Identify the blood parasite species.
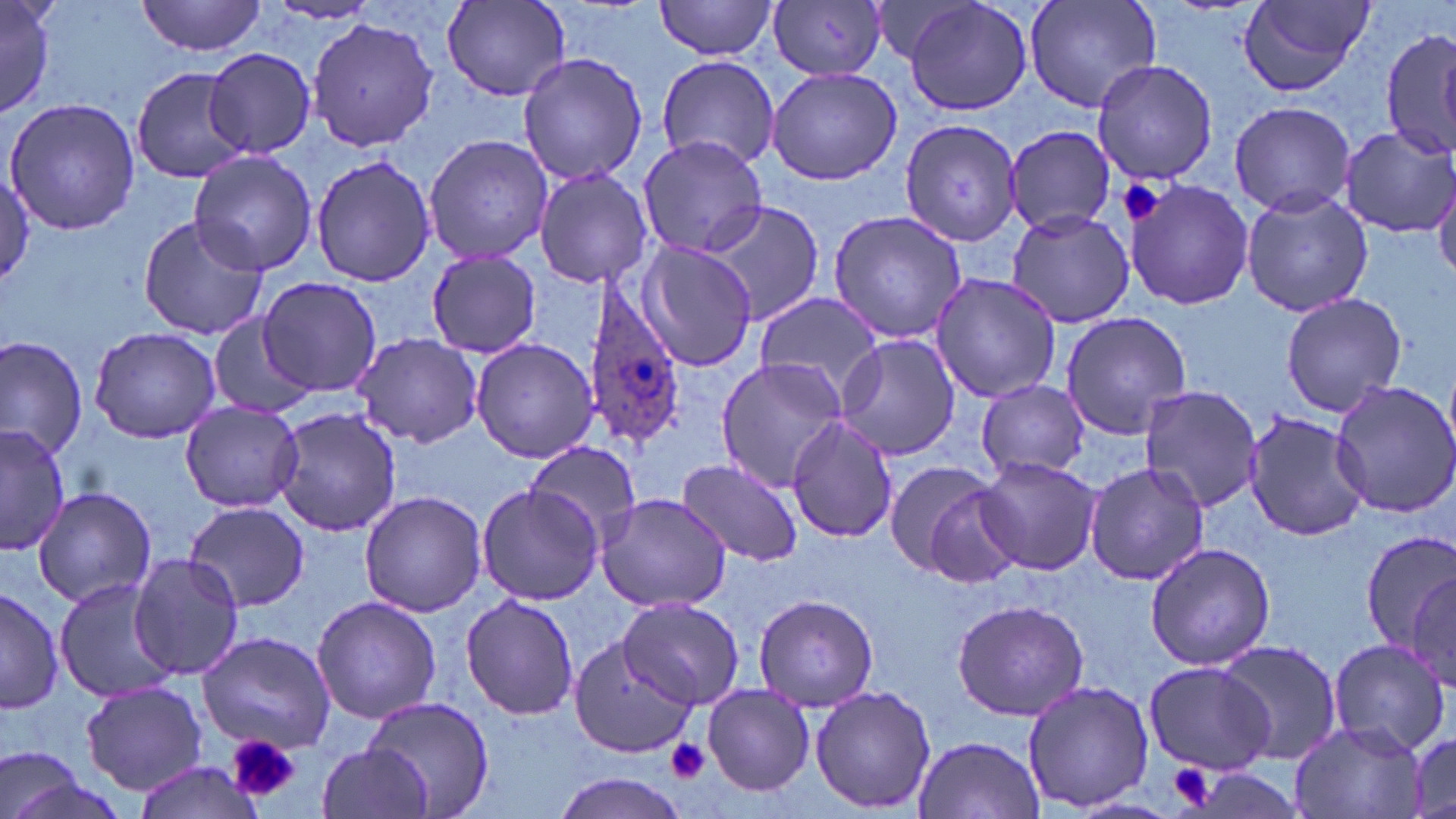

Plasmodium ovale.

Summary:
  - Coordinate format: approximate bounding boxes as [x1, y1, x2, y2] in pixels
  - Uninfected red blood cell locations: [0, 0, 56, 120], [137, 0, 268, 58], [655, 0, 779, 61], [901, 0, 1033, 116], [1024, 0, 1164, 115], [1234, 0, 1376, 100], [265, 2, 386, 28], [441, 2, 571, 102], [770, 2, 889, 82], [307, 16, 440, 154], [1379, 28, 1456, 161], [205, 48, 315, 159], [517, 53, 649, 186], [656, 57, 779, 169], [1091, 58, 1217, 186], [130, 64, 254, 185], [764, 65, 904, 185], [3, 96, 140, 235], [1229, 101, 1356, 215], [901, 116, 1022, 246], [1005, 124, 1114, 234], [1337, 126, 1455, 238], [423, 132, 553, 265], [637, 135, 770, 257], [189, 150, 319, 277], [310, 153, 437, 287], [0, 165, 34, 289], [533, 165, 655, 289], [1430, 172, 1456, 283], [1126, 176, 1255, 312], [1239, 188, 1373, 317], [701, 201, 822, 328], [827, 209, 966, 346], [1007, 209, 1136, 329], [137, 215, 268, 342], [638, 241, 758, 371], [425, 248, 543, 357], [930, 273, 1061, 403], [257, 276, 380, 395], [1280, 289, 1407, 418], [753, 290, 882, 398], [1060, 312, 1192, 439], [208, 314, 313, 420], [87, 323, 224, 443], [353, 333, 483, 449], [0, 334, 90, 461], [833, 335, 960, 460], [470, 338, 597, 463], [714, 358, 848, 491], [975, 378, 1091, 482], [1328, 379, 1456, 519], [1137, 386, 1263, 513], [179, 399, 305, 513], [272, 406, 403, 538], [1243, 412, 1371, 540], [787, 416, 899, 542], [0, 423, 71, 559], [524, 443, 642, 543], [672, 457, 805, 568], [976, 458, 1101, 576], [1084, 460, 1208, 586], [881, 462, 1010, 582], [475, 483, 603, 605], [30, 485, 161, 610], [359, 491, 486, 616], [594, 493, 734, 611], [183, 501, 311, 613], [1358, 529, 1456, 658], [1144, 541, 1276, 671], [129, 554, 247, 681], [54, 576, 187, 704], [2, 585, 63, 715], [460, 593, 580, 720], [753, 595, 881, 711], [311, 596, 442, 724], [618, 597, 743, 711], [950, 599, 1090, 720], [195, 629, 334, 755], [569, 636, 694, 758], [1326, 638, 1450, 753], [1214, 639, 1343, 762], [1142, 660, 1278, 775], [1021, 678, 1154, 814], [78, 681, 209, 791], [702, 683, 812, 794], [809, 683, 936, 814], [363, 698, 494, 819], [1287, 719, 1428, 819], [912, 733, 1046, 819], [1405, 735, 1455, 815], [0, 741, 91, 819], [317, 742, 434, 819], [133, 761, 264, 819], [551, 770, 697, 819]
  - Platelet locations: [1117, 179, 1167, 226], [226, 733, 299, 804], [665, 737, 710, 782], [1166, 760, 1218, 811]
  - Plasmodium ovale-infected red blood cell locations: [578, 277, 690, 449]
  - Modality: light microscopy
  - Image size: 1456×819 pixels
  - Field of view: single
  - Magnification: 1000x
  - Stain: May-Grünwald-Giemsa
  - Preparation: thin blood film